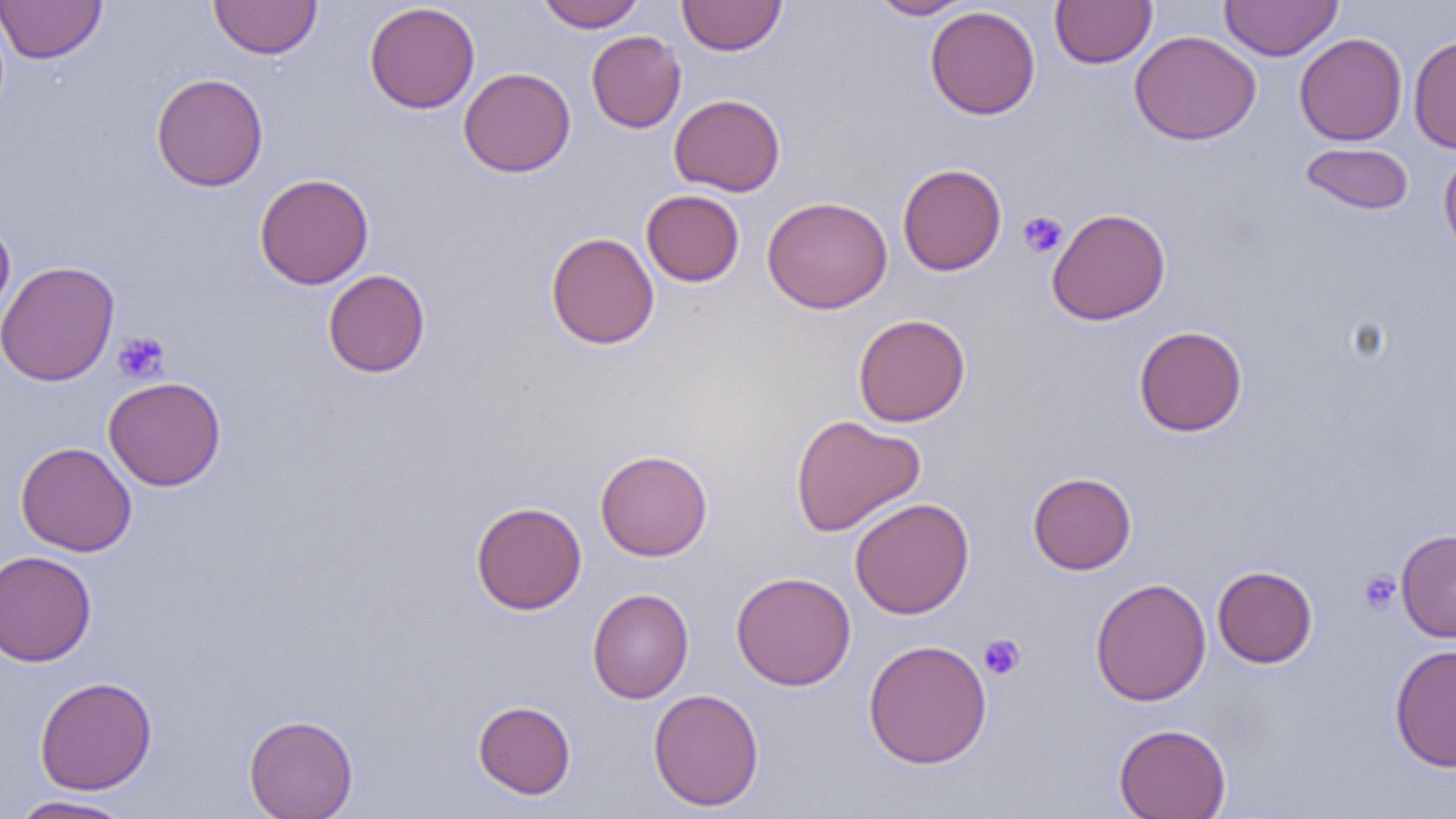
Approximate bounding boxes as [x1, y1, x2, y2] in pixels. Platelet locations: [1018, 211, 1068, 258], [112, 331, 170, 383], [1358, 570, 1401, 614], [978, 633, 1026, 680]. Uninfected red blood cell locations: [0, 0, 106, 64], [209, 0, 322, 59], [535, 0, 648, 31], [677, 0, 787, 56], [867, 0, 974, 19], [1050, 0, 1157, 69], [1219, 0, 1343, 60], [364, 2, 480, 114], [924, 5, 1041, 120], [586, 30, 686, 133], [1130, 30, 1261, 145], [1294, 32, 1407, 146], [1407, 35, 1456, 151], [459, 67, 576, 177], [151, 73, 268, 191], [669, 93, 786, 196], [1299, 142, 1414, 216], [1439, 148, 1456, 262], [897, 163, 1007, 276], [254, 173, 373, 289], [641, 190, 744, 287], [762, 195, 892, 314], [1046, 207, 1171, 325], [0, 219, 15, 327], [545, 231, 659, 350], [0, 260, 119, 386], [323, 269, 430, 378], [853, 314, 970, 427], [1133, 326, 1248, 436], [103, 376, 226, 491], [790, 414, 926, 537], [16, 442, 136, 556], [595, 449, 713, 561], [1027, 471, 1136, 575], [849, 497, 974, 619], [470, 501, 587, 615], [1396, 529, 1456, 643], [0, 550, 97, 666], [1212, 565, 1318, 668], [731, 571, 856, 690], [1090, 577, 1211, 706], [587, 588, 694, 703], [862, 639, 992, 768], [1389, 642, 1456, 772], [34, 676, 157, 795], [647, 688, 764, 812], [473, 700, 576, 799], [244, 714, 358, 818], [1114, 723, 1231, 819], [7, 795, 135, 818]. Slide-level diagnosis: no evidence of blood parasites. Image is 1456×819 pixels. Captured at 1000x magnification. One field of a larger specimen. Optical microscopy. Thin blood film.